Describe the morphology of the erythrocytes.
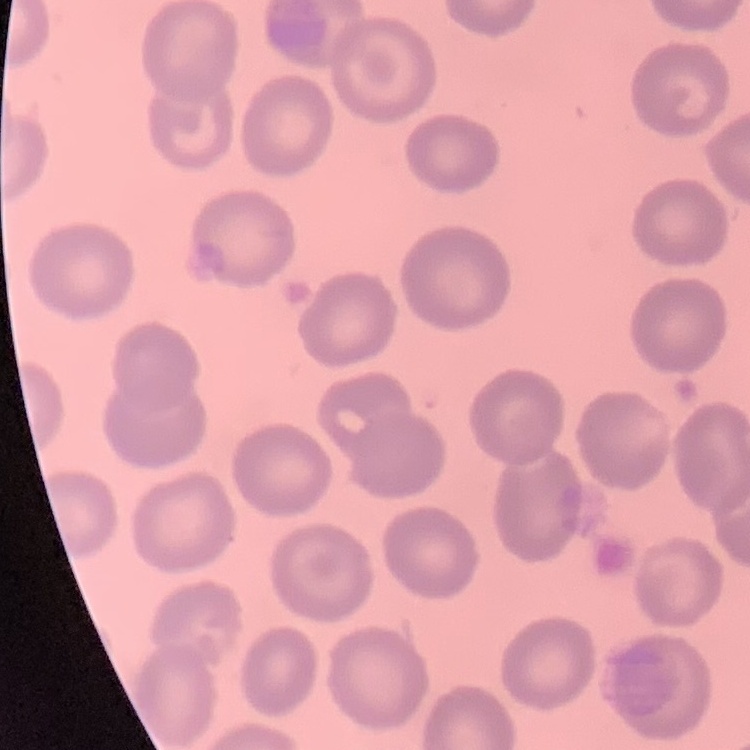
They show no rouleaux formation.

Stained with either Field's or Giemsa. Square crop of a larger photomicrograph. Thin peripheral smear.